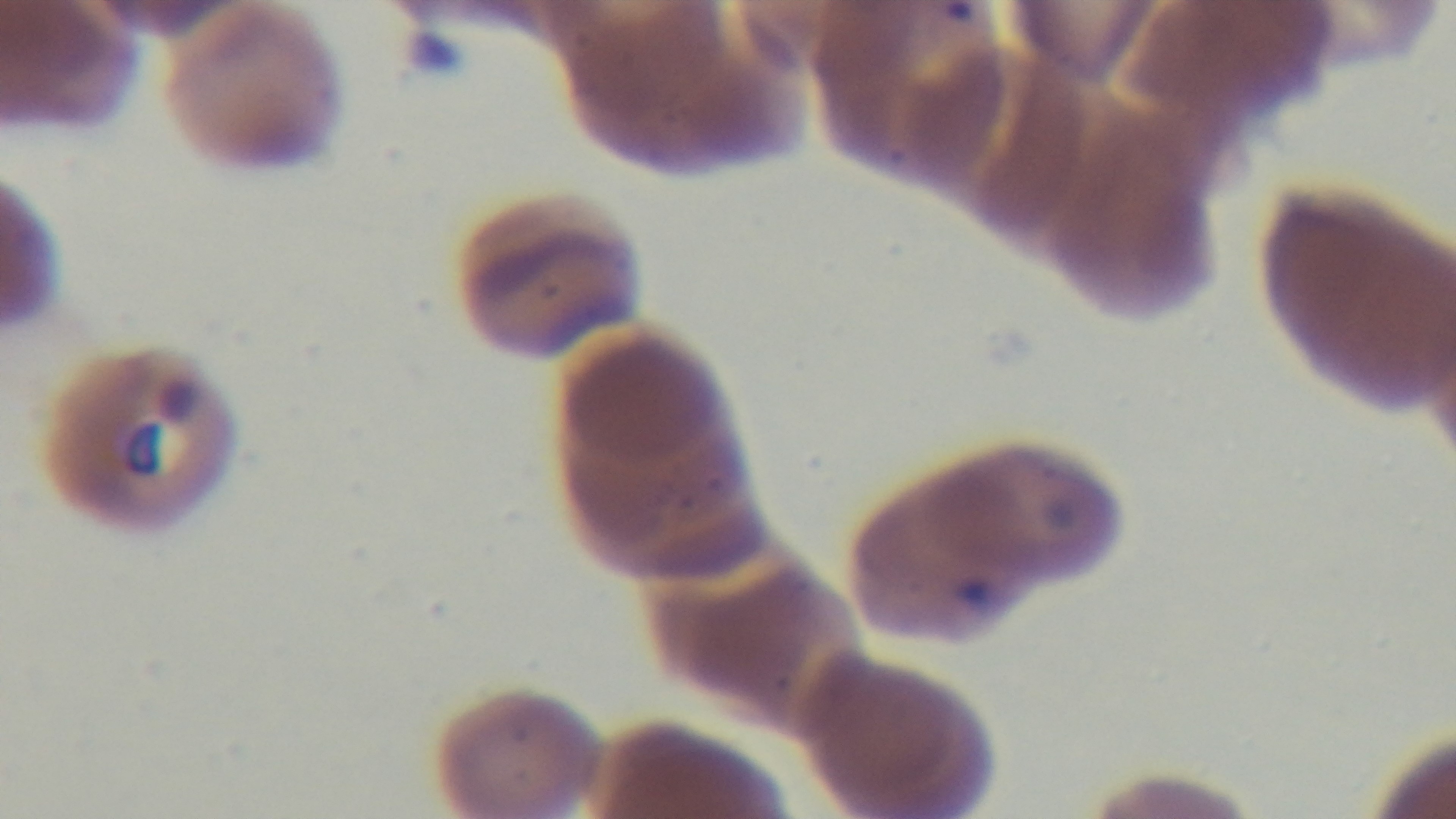 100x oil-immersion objective. Malaria status: infected. One field from the slide. Mounted 4K digital camera. Photomicrograph. Preparation: thin smear. Giemsa stain.